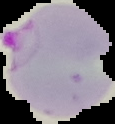
malaria status = parasitized
image type = segmented cell region on a black background
preparation = thin blood smear
image size = 115×124 pixels